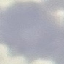

Summary:
  - Result: no malaria parasites seen
  - Image type: cell patch, automatically extracted from a larger field of view and resized to 64 × 64 pixels
  - Preparation: thin smear
  - Capture: smartphone camera at the microscope eyepiece
  - Stain: Giemsa